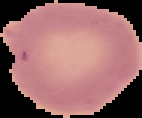 Result: negative for Plasmodium parasites. Image is 142×118 pixels. From a thin blood film. The area outside the segmented cell region is set to black.